Report the malaria status of this cell.
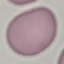
It is uninfected.

Summary:
  - Image type: automatically extracted cell patch, resized to 64 × 64 pixels
  - Capture: smartphone through the microscope eyepiece
  - Preparation: thin blood smear
  - Stain: Giemsa